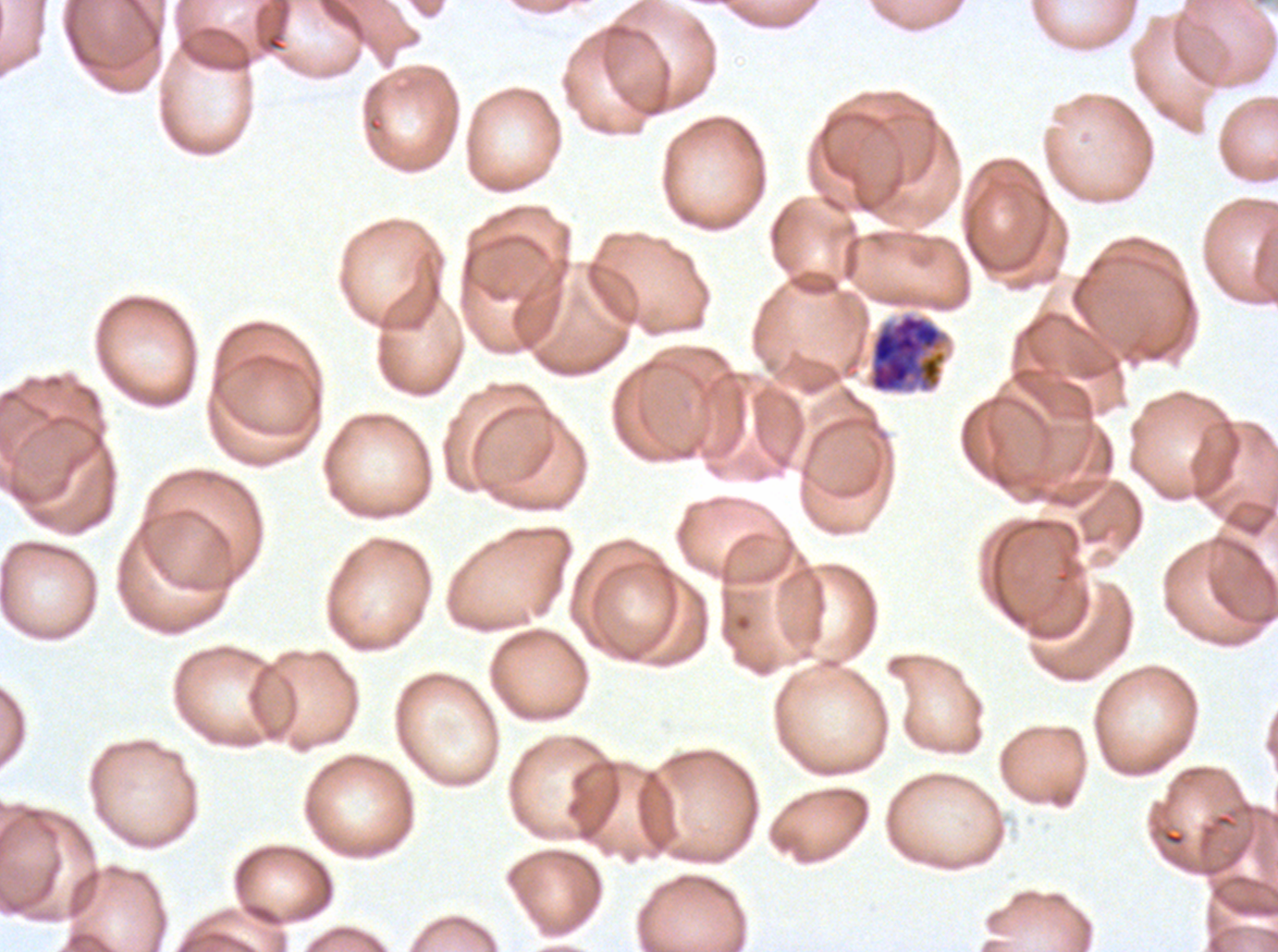

Approximate bounding boxes as {x1, y1, x2, y2} in pixels.
Summary:
  - Late schizont locations: {867, 312, 947, 394}
  - Field of view: sub-image separated from a larger composite
  - Stain: Giemsa
  - Image size: 1278×952 pixels
  - Preparation: thin blood smear
  - Specimen: Plasmodium falciparum from a patient in The Gambia, cultured ex vivo for 24 to 48 hours